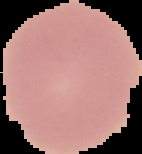 The area outside the segmented cell region is set to black. Result: no malaria parasites detected. Image is 142×154 pixels. From a thin blood film.